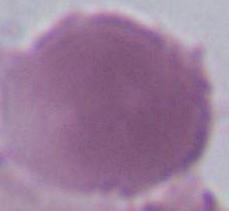 Micrograph. A red blood cell is seen. Captured at 1000x magnification.